Classify this cell by malaria status.
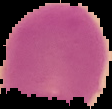

It is uninfected.

Image is 112×109 pixels. Cell region segmented out of the field of view; the surrounding area is masked to black. From a thin blood smear.